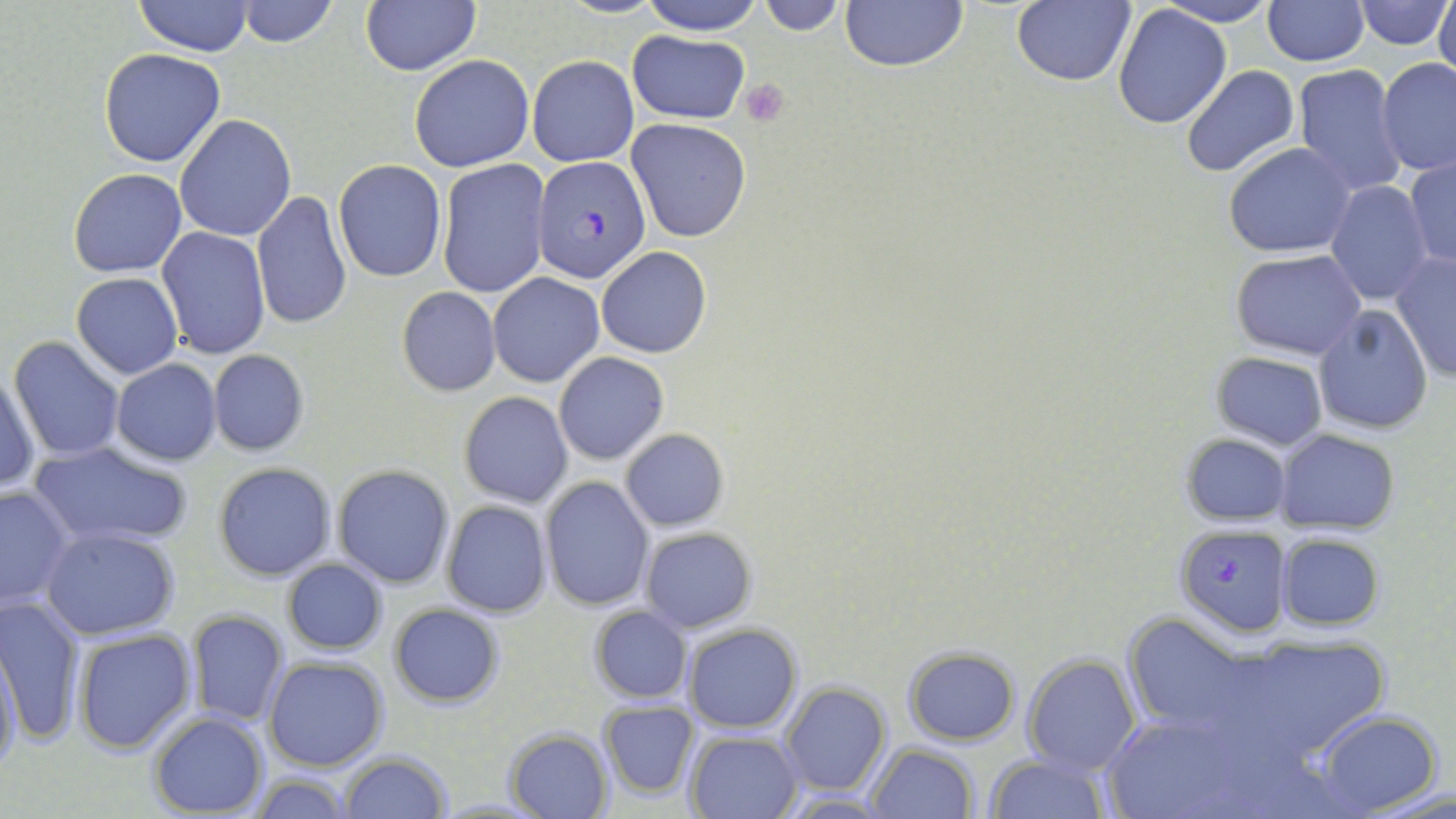

slide-level diagnosis = Plasmodium falciparum
uninfected red blood cell locations = approximate bounding boxes as named x1/y1/x2/y2 corners in pixels: (x1=133, y1=0, x2=254, y2=57), (x1=361, y1=0, x2=481, y2=75), (x1=637, y1=0, x2=765, y2=36), (x1=840, y1=0, x2=968, y2=72), (x1=1353, y1=0, x2=1451, y2=49), (x1=1435, y1=0, x2=1456, y2=84), (x1=235, y1=1, x2=338, y2=48), (x1=758, y1=1, x2=846, y2=35), (x1=1011, y1=1, x2=1136, y2=88), (x1=1156, y1=1, x2=1279, y2=26), (x1=1263, y1=1, x2=1369, y2=67), (x1=1113, y1=6, x2=1232, y2=129), (x1=626, y1=31, x2=748, y2=124), (x1=98, y1=48, x2=226, y2=168), (x1=408, y1=55, x2=534, y2=172), (x1=527, y1=56, x2=638, y2=168), (x1=1378, y1=58, x2=1456, y2=178), (x1=1179, y1=64, x2=1301, y2=178), (x1=1294, y1=64, x2=1409, y2=198), (x1=173, y1=114, x2=297, y2=242), (x1=625, y1=118, x2=751, y2=243), (x1=1225, y1=143, x2=1357, y2=258), (x1=1405, y1=156, x2=1455, y2=269), (x1=437, y1=159, x2=550, y2=298), (x1=333, y1=160, x2=446, y2=282), (x1=67, y1=169, x2=187, y2=278), (x1=1324, y1=182, x2=1433, y2=306), (x1=252, y1=190, x2=352, y2=330), (x1=156, y1=226, x2=270, y2=360), (x1=596, y1=246, x2=712, y2=359), (x1=1231, y1=249, x2=1367, y2=359), (x1=1390, y1=249, x2=1455, y2=382), (x1=72, y1=271, x2=183, y2=378), (x1=488, y1=273, x2=605, y2=388), (x1=397, y1=286, x2=501, y2=397), (x1=1313, y1=305, x2=1434, y2=433), (x1=9, y1=336, x2=125, y2=462), (x1=207, y1=350, x2=310, y2=457), (x1=554, y1=351, x2=669, y2=465), (x1=1209, y1=352, x2=1329, y2=451), (x1=112, y1=358, x2=221, y2=464), (x1=1, y1=371, x2=40, y2=496), (x1=458, y1=390, x2=573, y2=508), (x1=619, y1=429, x2=730, y2=532), (x1=1277, y1=429, x2=1398, y2=532), (x1=1181, y1=433, x2=1290, y2=526), (x1=28, y1=440, x2=195, y2=550), (x1=214, y1=462, x2=336, y2=580), (x1=333, y1=465, x2=453, y2=589), (x1=540, y1=476, x2=653, y2=612), (x1=0, y1=485, x2=75, y2=608), (x1=441, y1=499, x2=552, y2=617), (x1=640, y1=526, x2=759, y2=633), (x1=42, y1=527, x2=181, y2=641), (x1=1276, y1=533, x2=1386, y2=631), (x1=281, y1=559, x2=387, y2=654), (x1=0, y1=593, x2=86, y2=744), (x1=388, y1=603, x2=504, y2=707), (x1=588, y1=605, x2=691, y2=705), (x1=186, y1=609, x2=289, y2=725), (x1=1123, y1=614, x2=1256, y2=739), (x1=682, y1=623, x2=803, y2=733), (x1=1174, y1=625, x2=1404, y2=775), (x1=73, y1=628, x2=196, y2=753), (x1=0, y1=643, x2=23, y2=778), (x1=902, y1=647, x2=1019, y2=745), (x1=1022, y1=653, x2=1140, y2=774), (x1=263, y1=657, x2=387, y2=772), (x1=780, y1=681, x2=893, y2=797), (x1=597, y1=700, x2=699, y2=800), (x1=1311, y1=710, x2=1444, y2=816), (x1=148, y1=712, x2=268, y2=817), (x1=1105, y1=712, x2=1254, y2=819), (x1=506, y1=728, x2=613, y2=818), (x1=686, y1=730, x2=803, y2=817), (x1=869, y1=742, x2=978, y2=818), (x1=339, y1=751, x2=452, y2=818), (x1=986, y1=754, x2=1111, y2=817), (x1=251, y1=773, x2=356, y2=818), (x1=1362, y1=779, x2=1456, y2=817)
platelet locations = approximate bounding boxes as named x1/y1/x2/y2 corners in pixels: (x1=739, y1=79, x2=789, y2=126)
preparation = thin blood film
stain = May-Grünwald-Giemsa
field of view = one of a larger specimen
modality = light microscopy
magnification = 1000x
image size = 1456×819 pixels
Plasmodium falciparum-infected red blood cell locations = approximate bounding boxes as named x1/y1/x2/y2 corners in pixels: (x1=531, y1=156, x2=651, y2=283), (x1=1174, y1=523, x2=1290, y2=636)